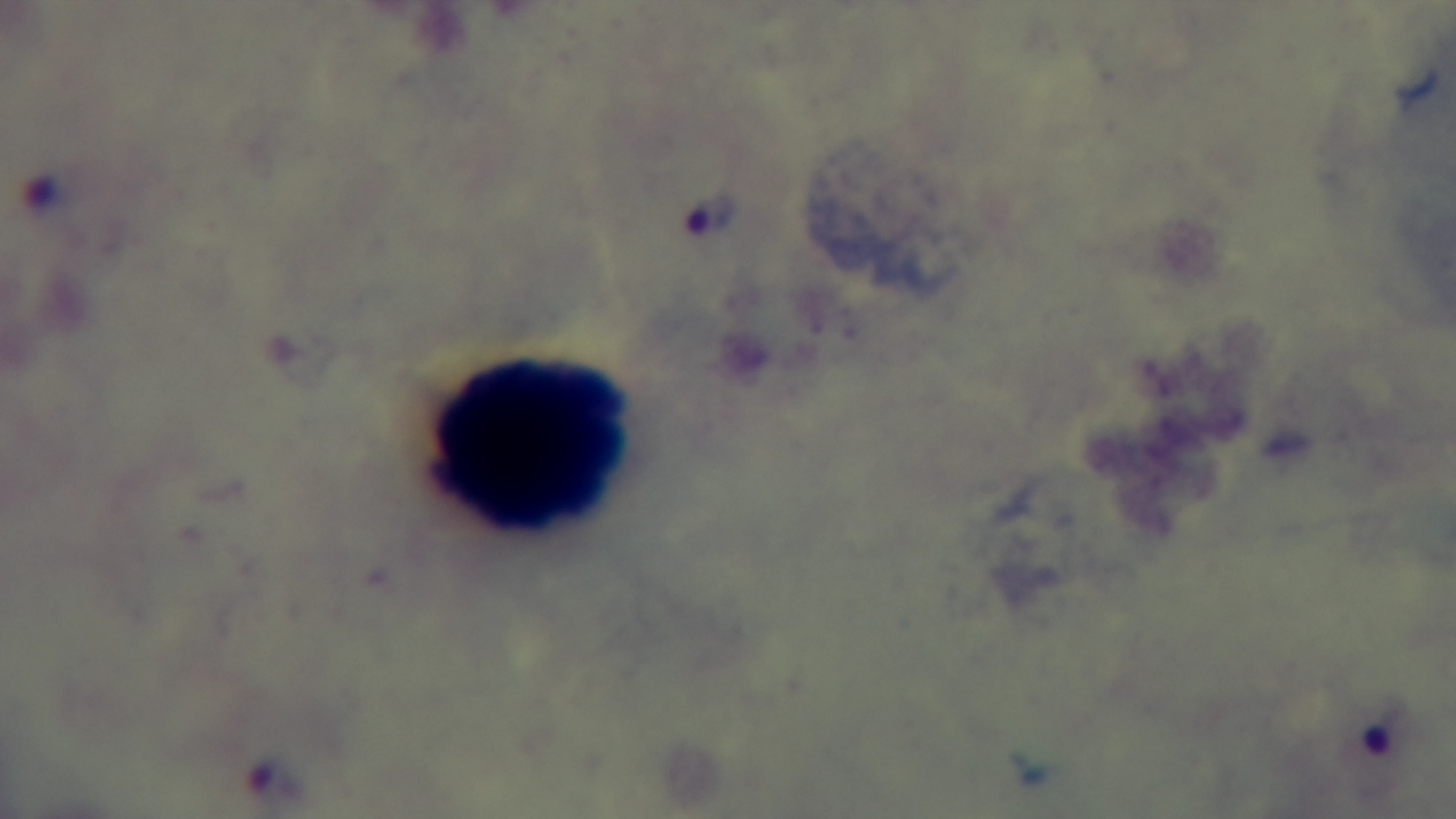
Summary:
  - Preparation: thick
  - Malaria status: infected
  - Field of view: single
  - Modality: light microscopy
  - Capture: mounted 4K digital camera
  - Objective: 100x oil immersion
  - Stain: Giemsa